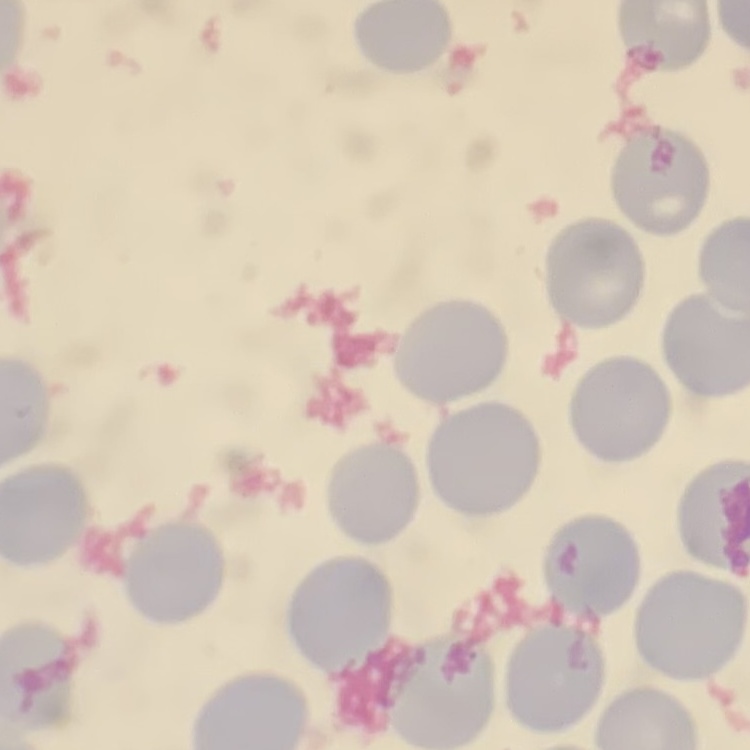
The erythrocytes show no rouleaux formation. Stained with either Field's or Giemsa. Square crop of a larger photomicrograph. Thin blood film.